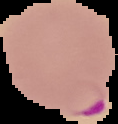

Summary:
  - Result: malaria parasites identified
  - Image type: segmented cell region on a black background
  - Preparation: thin blood film
  - Image size: 118×124 pixels